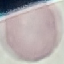

result = no malaria parasites seen
stain = Giemsa
image type = automatically extracted cell patch, resized to 64 × 64 pixels
preparation = thin smear
capture = smartphone through the microscope eyepiece